Report the malaria status of this cell.
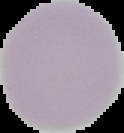

Uninfected.

Segmented cell region on a black background. From a thin blood film. Image is 124×133 pixels.